State the preparation type.
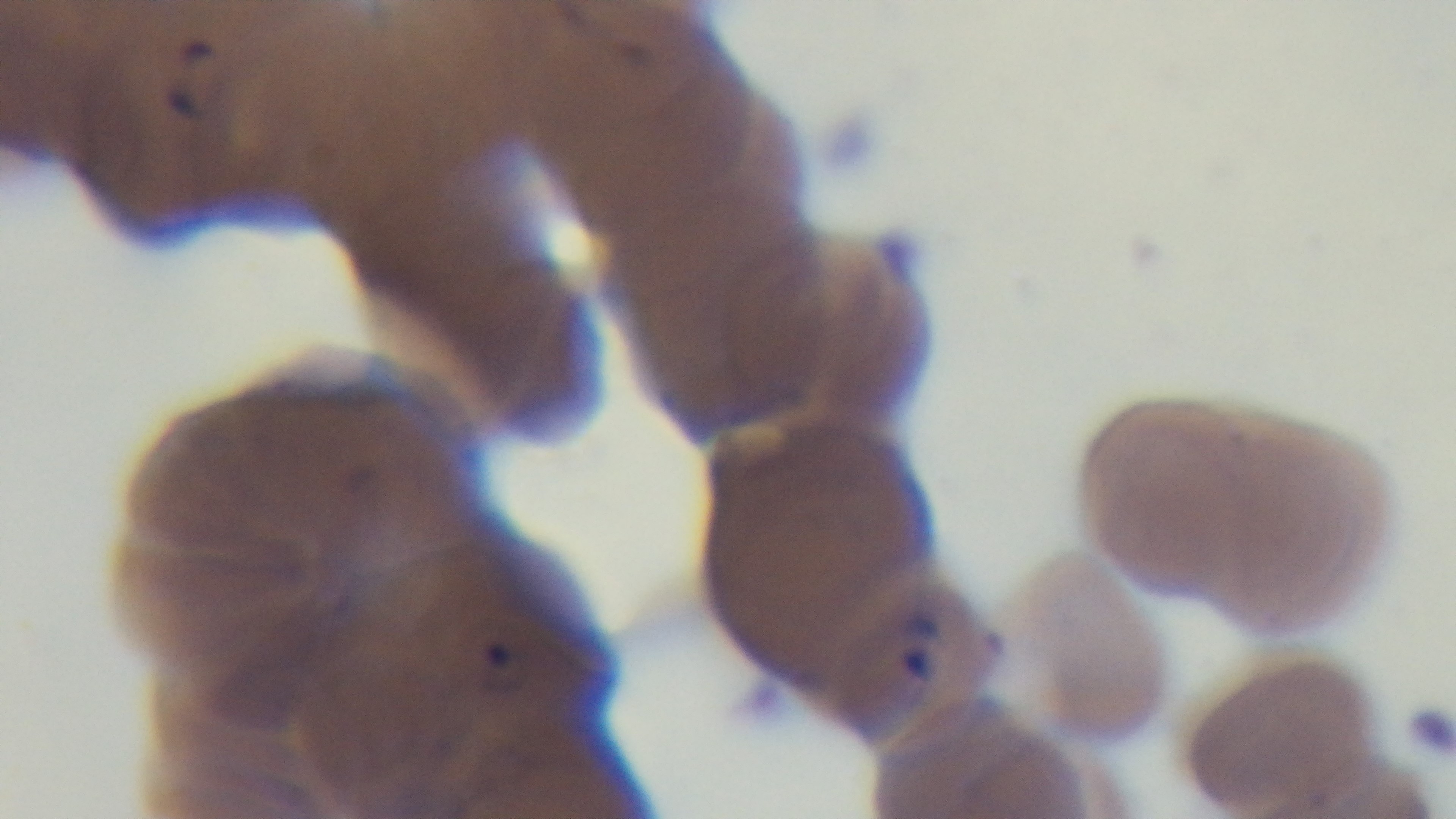

Thin.

Oil-immersion objective, 100x. Giemsa-stained. Photomicrograph. Malaria status: positive. One field from the slide. Mounted 4K digital camera.